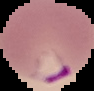

From a thin blood smear. Malaria status: parasitized. Segmented cell region on a black background. Image is 94×91 pixels.